Give a bounding box for every Plasmodium parasite.
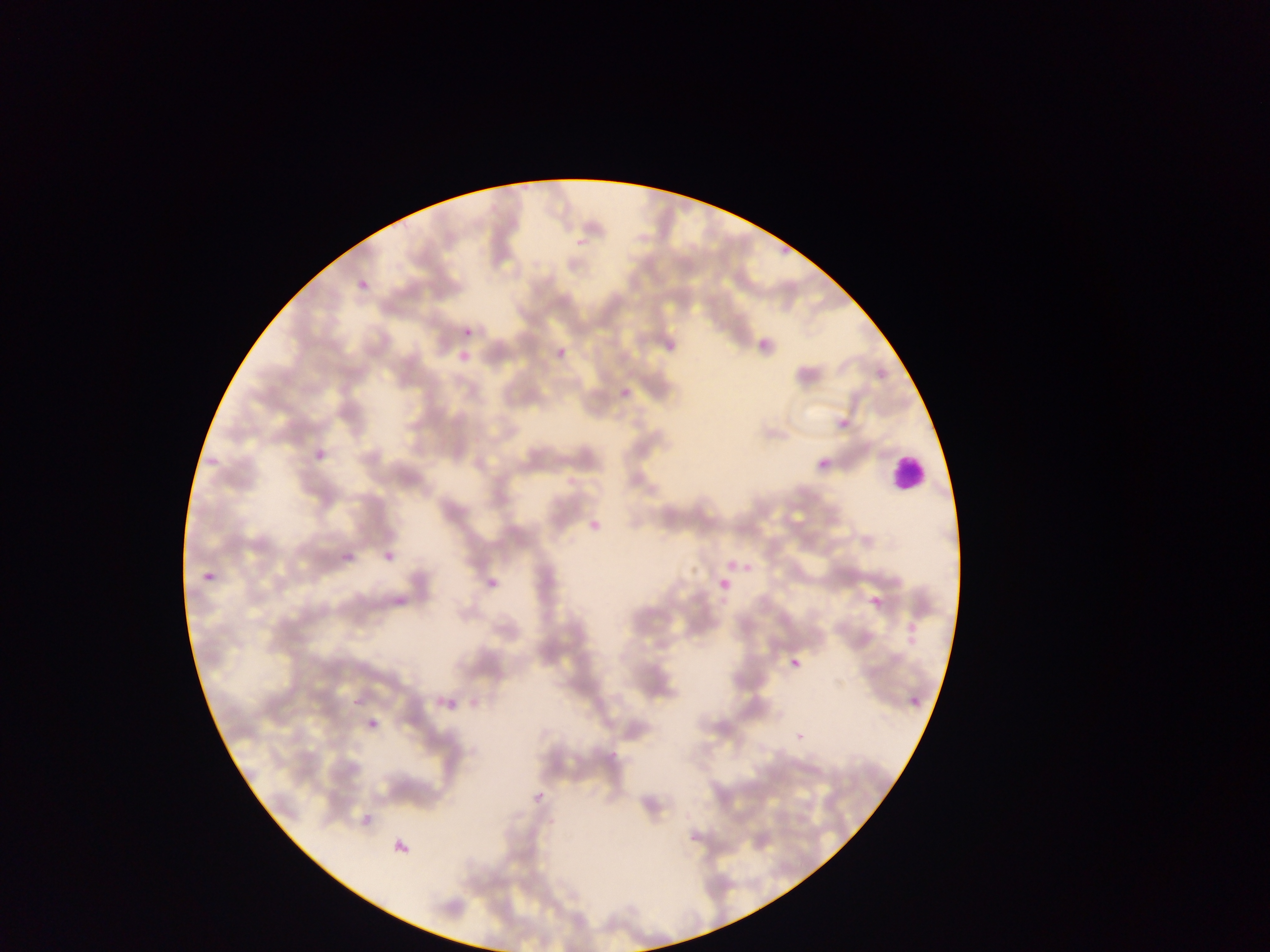

Approximate bounding boxes as left top right bottom in pixels.
Plasmodium parasites: 358 280 370 288; 463 328 473 337; 752 338 764 356; 655 339 673 357; 556 346 567 358; 454 353 475 365; 795 362 816 383; 877 370 886 378; 607 378 633 409; 840 419 850 429; 311 450 322 463; 819 460 829 469; 587 507 611 543; 378 544 396 565; 341 551 356 564; 738 555 756 581; 719 559 747 581; 203 562 216 583; 481 571 506 591; 716 578 729 597; 857 588 876 616; 393 593 403 605; 899 606 933 648; 785 649 804 664; 344 689 366 703; 440 693 455 708; 908 694 924 707; 360 717 373 736; 527 792 544 807; 354 810 369 830; 380 822 412 869.

Leukocyte locations: 888 453 927 494. Mobile-phone photograph taken through the microscope. One field of view. Thin blood film. Collected in Ghana. Image is 1270×952 pixels.